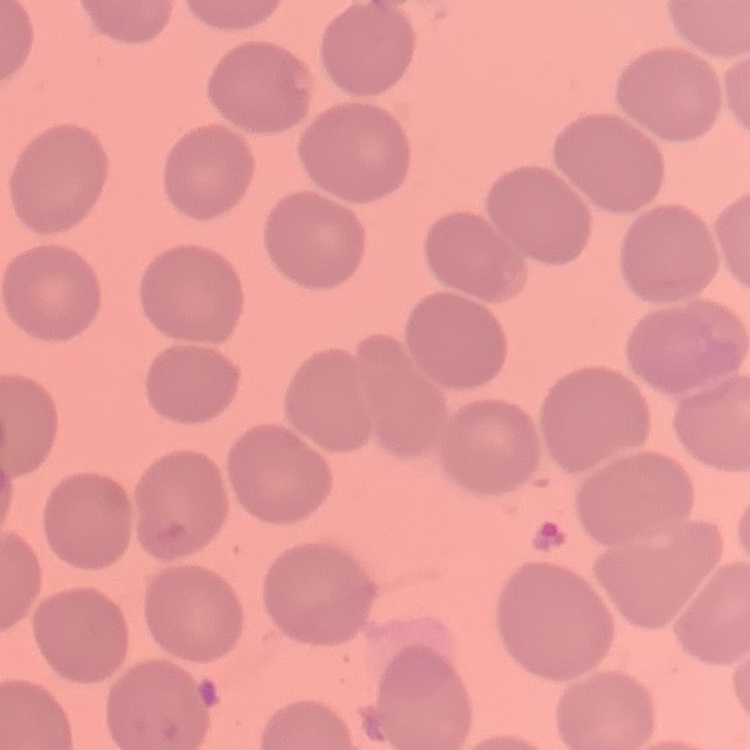
erythrocyte_morphology: no rouleaux formation
preparation: thin blood film
stain: Field's or Giemsa
image_type: one tile cut from a larger photomicrograph